Report the malaria status of this cell.
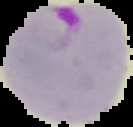

It is parasitized.

From a thin blood film. Segmented cell region on a black background. Image is 133×127 pixels.